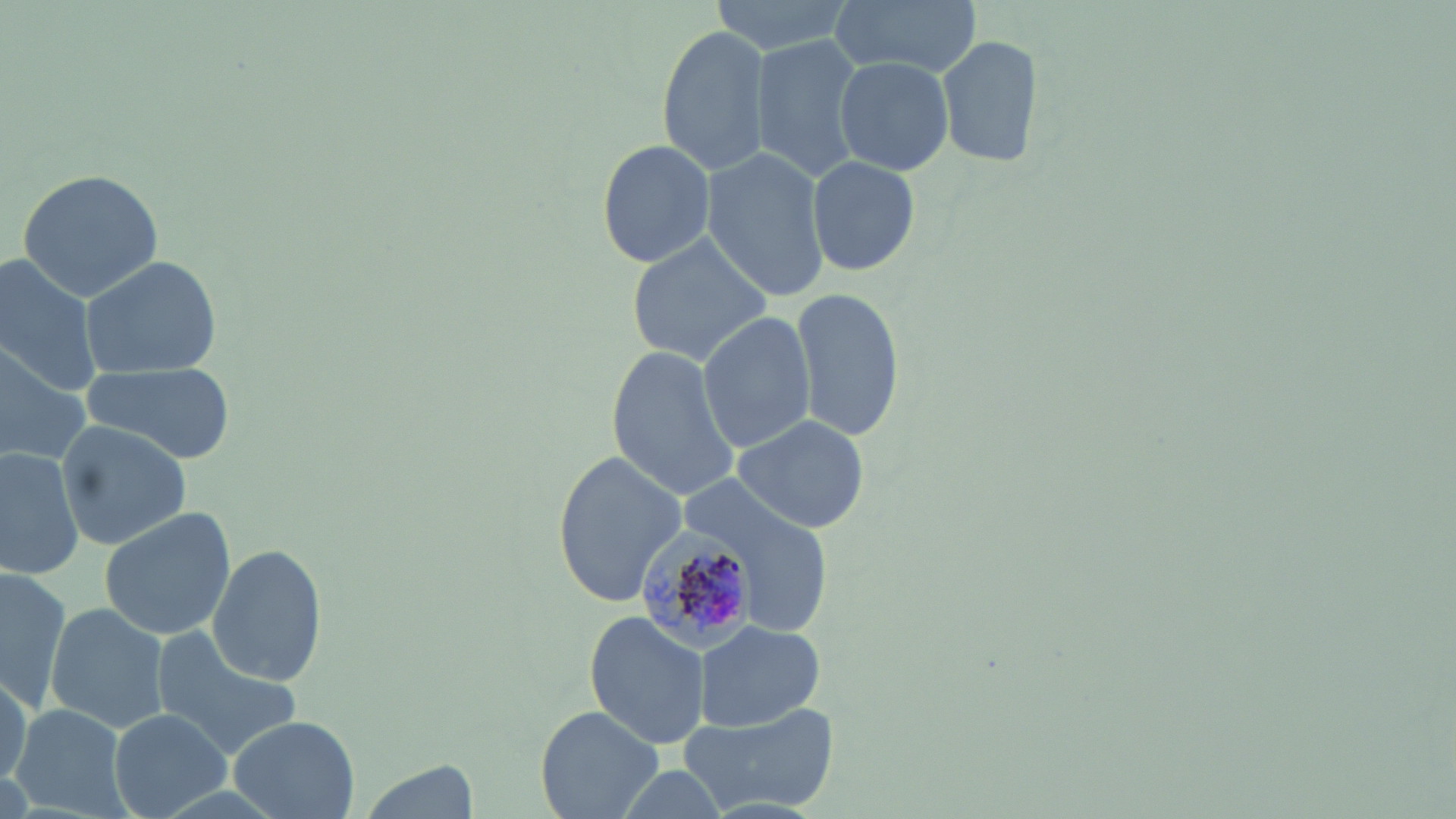
Summary:
  - Coordinate format: approximate bounding boxes as (x1,y1)-(x2,y2) corner pairs in pixels
  - Uninfected red blood cell locations: (706,0)-(855,56), (827,0)-(986,80), (658,23)-(771,178), (937,33)-(1042,170), (751,35)-(868,183), (836,57)-(953,174), (595,138)-(716,269), (701,148)-(832,300), (806,154)-(921,278), (16,167)-(165,300), (625,231)-(773,365), (0,251)-(107,398), (79,252)-(225,379), (790,287)-(905,443), (695,312)-(816,452), (0,340)-(92,464), (605,345)-(741,503), (77,364)-(237,463), (733,413)-(872,533), (55,419)-(190,548), (0,447)-(82,581), (552,449)-(686,609), (667,468)-(839,636), (98,506)-(235,643), (208,543)-(327,689), (0,564)-(72,706), (44,602)-(169,734), (586,611)-(708,750), (694,620)-(823,732), (152,625)-(304,756), (0,671)-(31,799), (678,699)-(839,816), (10,702)-(131,819), (535,705)-(663,819), (108,708)-(230,818), (227,714)-(360,818), (605,763)-(734,819)
  - Plasmodium malariae-infected red blood cell locations: (634,527)-(766,649)
  - Slide-level diagnosis: Plasmodium malariae
  - Image size: 1456×819 pixels
  - Modality: light microscopy
  - Field of view: single
  - Preparation: thin blood smear
  - Magnification: 1000x
  - Stain: May-Grünwald-Giemsa